Identify the blood parasite species.
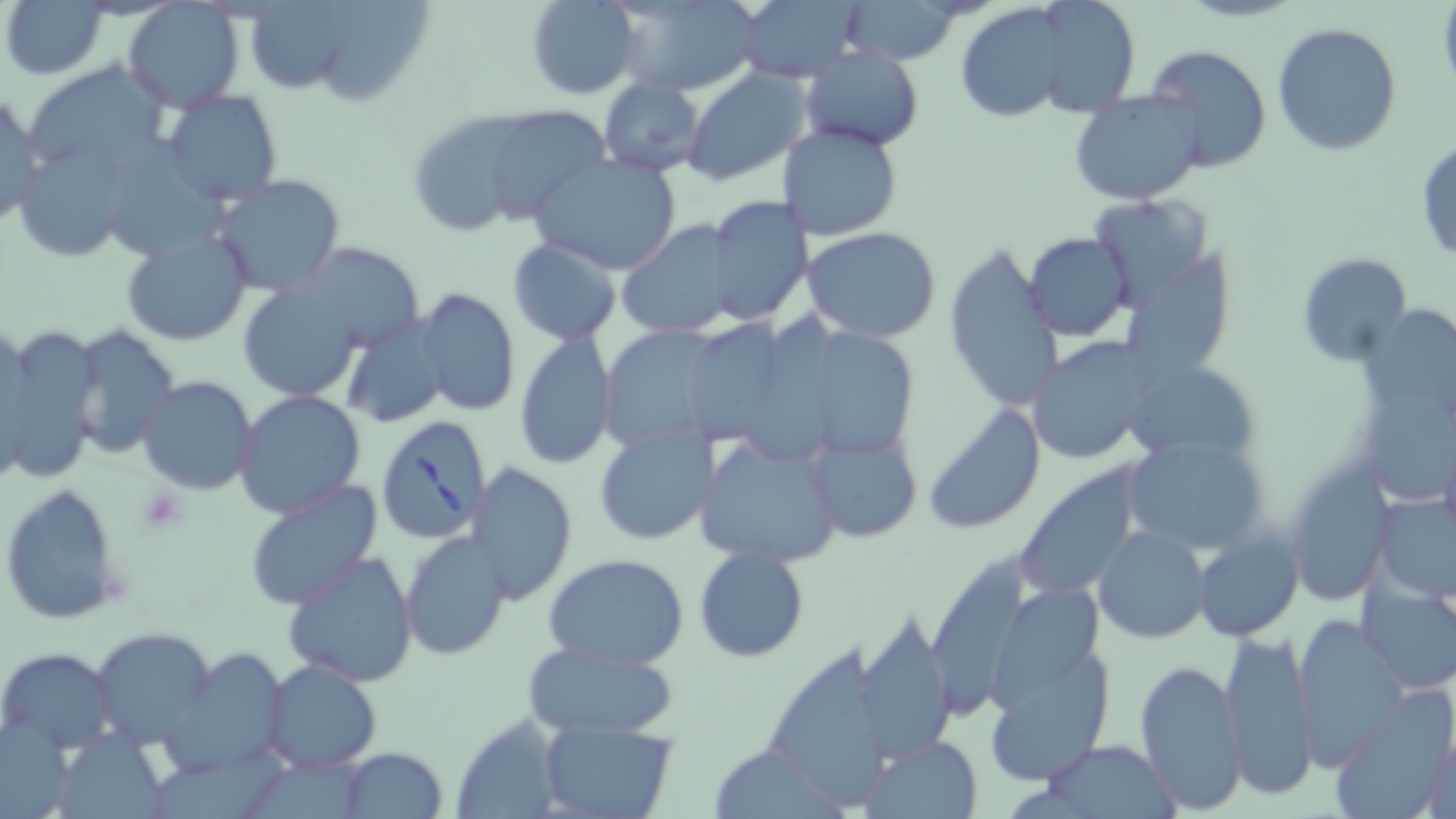
Babesia divergens.

uninfected_red_blood_cell_locations: 'approximate bounding boxes as named x1/y1/x2/y2 corners in pixels: (x1=3, y1=0, x2=111, y2=80), (x1=525, y1=0, x2=641, y2=99), (x1=609, y1=0, x2=762, y2=96), (x1=255, y1=1, x2=357, y2=92), (x1=321, y1=1, x2=432, y2=106), (x1=732, y1=1, x2=863, y2=85), (x1=841, y1=2, x2=962, y2=65), (x1=123, y1=3, x2=243, y2=114), (x1=955, y1=6, x2=1074, y2=124), (x1=1272, y1=22, x2=1401, y2=156), (x1=127, y1=43, x2=250, y2=183), (x1=801, y1=44, x2=923, y2=150), (x1=1143, y1=44, x2=1272, y2=173), (x1=23, y1=61, x2=174, y2=179), (x1=683, y1=69, x2=809, y2=184), (x1=598, y1=77, x2=705, y2=178), (x1=0, y1=90, x2=46, y2=228), (x1=159, y1=91, x2=284, y2=209), (x1=1070, y1=91, x2=1203, y2=205), (x1=473, y1=108, x2=609, y2=227), (x1=416, y1=110, x2=560, y2=231), (x1=790, y1=121, x2=921, y2=343), (x1=777, y1=123, x2=904, y2=242), (x1=1414, y1=139, x2=1456, y2=265), (x1=12, y1=140, x2=134, y2=262), (x1=529, y1=152, x2=684, y2=277), (x1=213, y1=175, x2=345, y2=297), (x1=702, y1=195, x2=814, y2=326), (x1=1086, y1=195, x2=1213, y2=303), (x1=616, y1=219, x2=740, y2=340), (x1=119, y1=226, x2=253, y2=347), (x1=802, y1=229, x2=943, y2=345), (x1=1023, y1=233, x2=1133, y2=340), (x1=506, y1=239, x2=623, y2=345), (x1=293, y1=241, x2=427, y2=354), (x1=943, y1=241, x2=1062, y2=418), (x1=1125, y1=244, x2=1247, y2=386), (x1=1296, y1=251, x2=1413, y2=365), (x1=238, y1=282, x2=364, y2=403), (x1=416, y1=288, x2=520, y2=417), (x1=339, y1=316, x2=450, y2=430), (x1=0, y1=323, x2=103, y2=484), (x1=67, y1=328, x2=183, y2=459), (x1=513, y1=331, x2=618, y2=469), (x1=1026, y1=337, x2=1156, y2=465), (x1=1129, y1=359, x2=1260, y2=466), (x1=136, y1=376, x2=257, y2=496), (x1=233, y1=390, x2=367, y2=518), (x1=925, y1=404, x2=1046, y2=534), (x1=593, y1=426, x2=716, y2=545), (x1=806, y1=429, x2=922, y2=542), (x1=1120, y1=432, x2=1267, y2=557), (x1=695, y1=434, x2=844, y2=566), (x1=466, y1=461, x2=577, y2=605), (x1=1015, y1=461, x2=1144, y2=601), (x1=1287, y1=463, x2=1391, y2=607), (x1=242, y1=479, x2=384, y2=610), (x1=1, y1=483, x2=125, y2=626), (x1=1373, y1=492, x2=1456, y2=599), (x1=1094, y1=526, x2=1210, y2=643), (x1=400, y1=532, x2=514, y2=659), (x1=1195, y1=533, x2=1301, y2=641), (x1=694, y1=546, x2=809, y2=662), (x1=281, y1=550, x2=421, y2=687), (x1=926, y1=551, x2=1034, y2=723), (x1=542, y1=553, x2=691, y2=672), (x1=1360, y1=581, x2=1456, y2=694), (x1=979, y1=612, x2=1116, y2=794), (x1=856, y1=613, x2=956, y2=764), (x1=1291, y1=614, x2=1407, y2=769), (x1=90, y1=628, x2=217, y2=747), (x1=1218, y1=628, x2=1319, y2=799), (x1=772, y1=635, x2=892, y2=808), (x1=522, y1=641, x2=678, y2=738), (x1=1, y1=648, x2=118, y2=752), (x1=164, y1=649, x2=287, y2=775), (x1=1134, y1=657, x2=1247, y2=813), (x1=261, y1=659, x2=383, y2=771), (x1=1330, y1=690, x2=1456, y2=817), (x1=3, y1=715, x2=87, y2=819), (x1=449, y1=715, x2=566, y2=819), (x1=539, y1=721, x2=677, y2=818), (x1=55, y1=727, x2=180, y2=819), (x1=1419, y1=733, x2=1455, y2=819), (x1=864, y1=735, x2=983, y2=818), (x1=1046, y1=739, x2=1177, y2=816), (x1=708, y1=741, x2=850, y2=819), (x1=338, y1=746, x2=448, y2=818), (x1=159, y1=749, x2=296, y2=819), (x1=254, y1=749, x2=382, y2=819)'
babesia_divergens_infected_red_blood_cell_locations: 'approximate bounding boxes as named x1/y1/x2/y2 corners in pixels: (x1=375, y1=414, x2=492, y2=545)'
field_of_view: single
modality: light microscopy
platelet_locations: 'approximate bounding boxes as named x1/y1/x2/y2 corners in pixels: (x1=137, y1=486, x2=188, y2=532)'
magnification: 1000x
preparation: thin blood film
image_size: 1456×819 pixels
stain: May-Grünwald-Giemsa